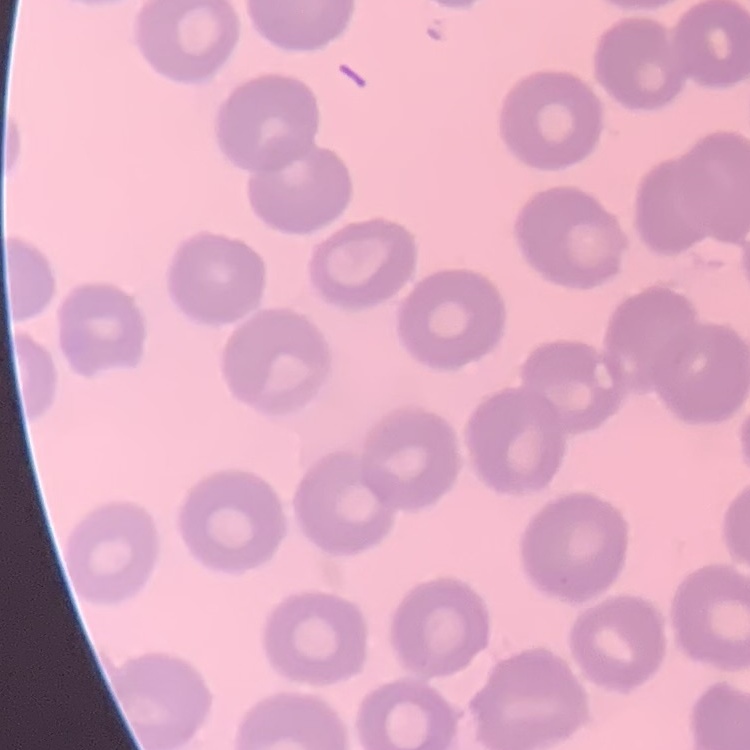

Summary:
  - Erythrocyte morphology: no rouleaux formation
  - Image type: one tile cut from a larger photomicrograph
  - Preparation: thin blood smear
  - Stain: Field's or Giemsa